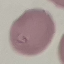 Result: negative for malaria parasites. Giemsa stain. Acquired by smartphone through the microscope eyepiece. Automatically extracted cell patch, resized to 64 × 64 pixels. Thin blood smear.